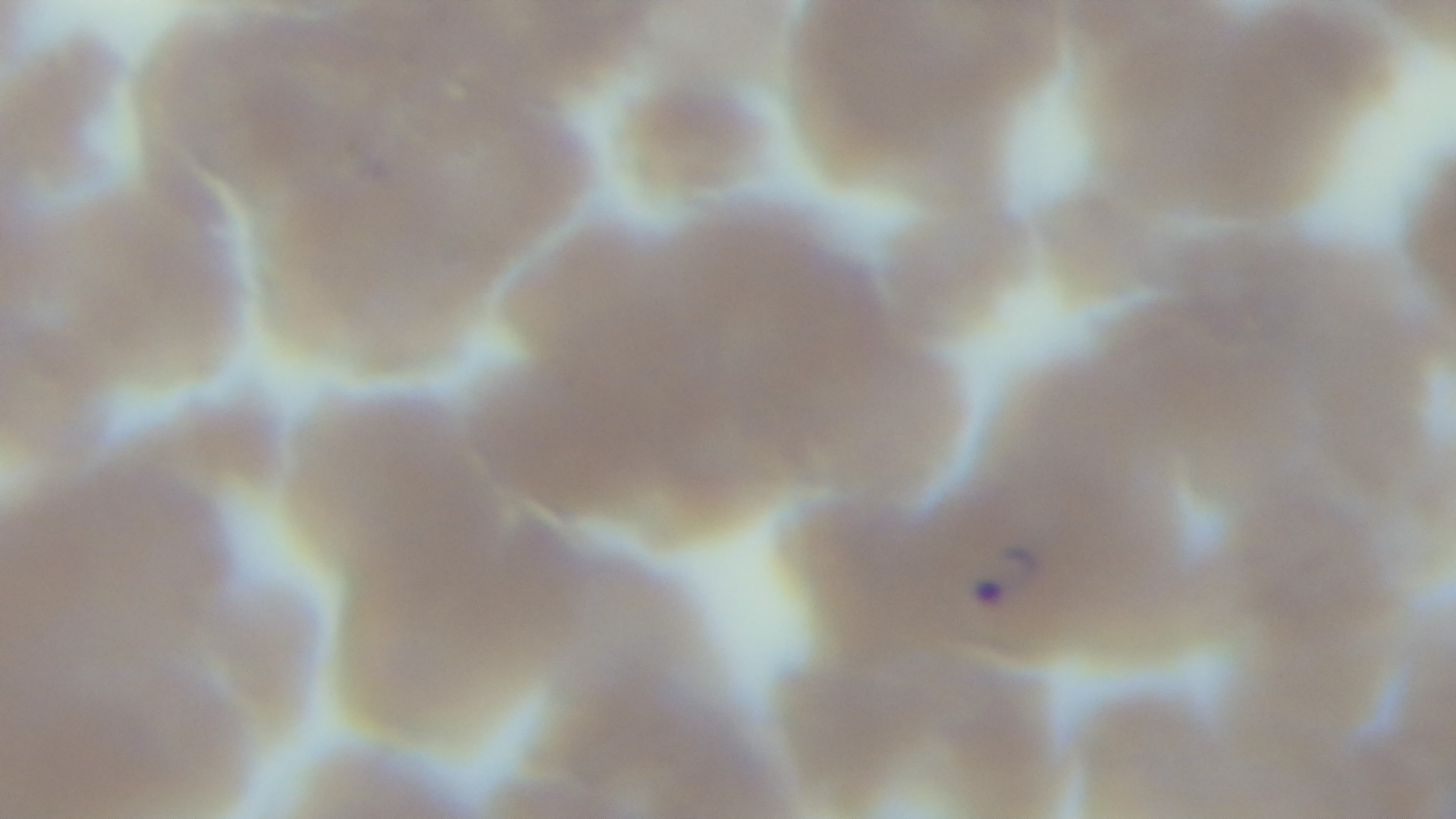
Malaria status: infected. Single field of view. Photomicrograph. Captured with a mounted 4K digital camera. Oil-immersion objective, 100x. Giemsa stain. Preparation: thin.